Give the position of every malaria parasite.
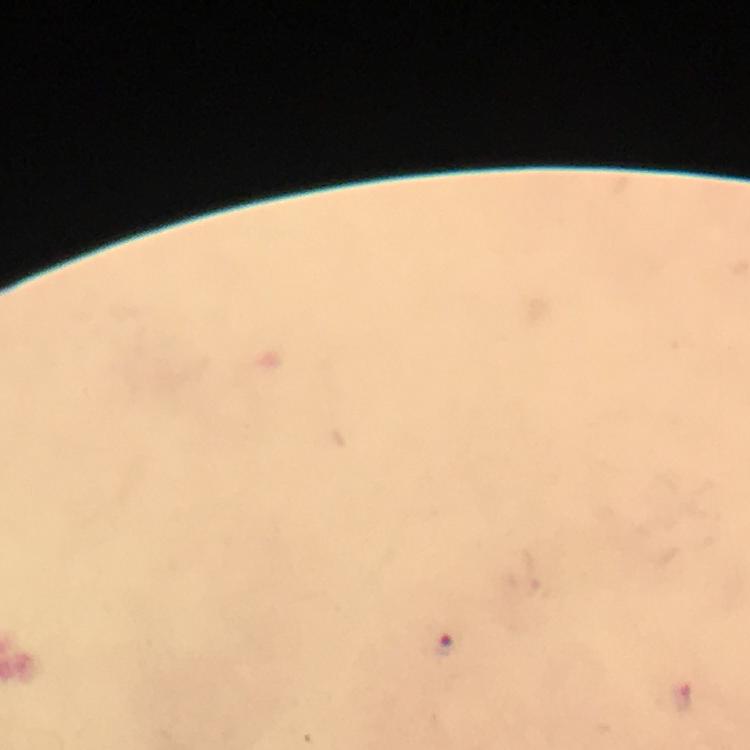
Approximate centers as (x, y) in pixels.
Malaria parasites: (439, 645), (683, 698).

Smartphone photograph taken through a microscope. From a diagnostic examination for malaria. Giemsa-stained preparation. Immersion oil was used. Thick blood smear. Image is 750×750 pixels. 100x magnification. A crop from one field of view.